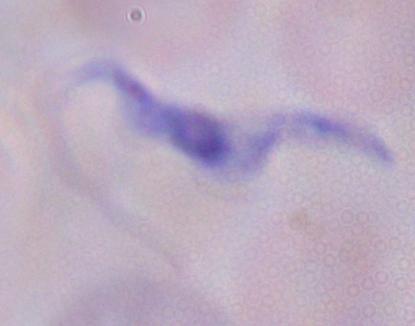
Summary:
  - Identification: trypanosome
  - Magnification: 1000x
  - Modality: micrograph